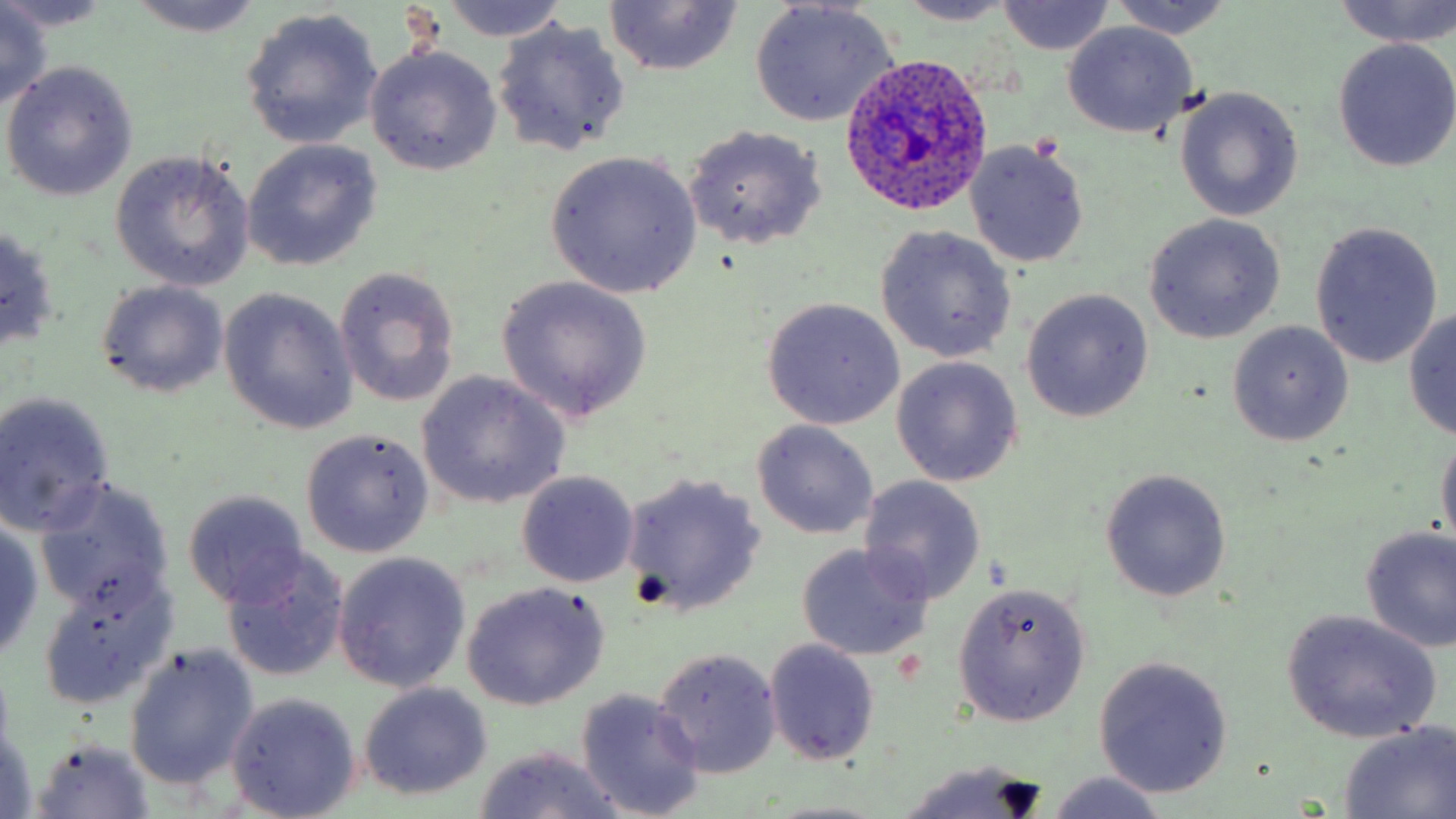 Approximate bounding boxes as [x1, y1, x2, y2] in pixels. Uninfected red blood cell locations: [123, 0, 264, 38], [1106, 0, 1238, 40], [0, 1, 113, 34], [436, 1, 574, 43], [1333, 1, 1456, 49], [602, 2, 742, 76], [895, 2, 1019, 26], [998, 2, 1113, 54], [0, 3, 53, 109], [750, 4, 898, 125], [239, 8, 385, 150], [491, 20, 630, 158], [1062, 22, 1197, 137], [1331, 39, 1456, 174], [365, 44, 502, 176], [3, 60, 139, 200], [1175, 89, 1302, 219], [682, 124, 828, 250], [964, 138, 1091, 269], [243, 140, 382, 271], [111, 150, 255, 291], [545, 151, 702, 299], [1143, 214, 1285, 343], [1308, 221, 1443, 370], [0, 225, 61, 353], [874, 226, 1016, 363], [335, 267, 460, 407], [495, 275, 654, 422], [96, 280, 230, 399], [1021, 288, 1154, 423], [219, 289, 359, 436], [761, 298, 905, 431], [1402, 307, 1456, 437], [1227, 322, 1354, 447], [891, 356, 1024, 487], [416, 372, 568, 509], [0, 393, 116, 537], [749, 419, 879, 540], [301, 429, 434, 558], [1436, 431, 1456, 557], [1099, 468, 1232, 603], [516, 471, 639, 587], [621, 473, 766, 619], [858, 475, 987, 604], [37, 480, 174, 618], [182, 489, 310, 610], [0, 517, 46, 665], [1357, 525, 1456, 654], [796, 543, 934, 662], [223, 552, 348, 682], [332, 552, 470, 694], [38, 577, 171, 708], [953, 582, 1090, 727], [464, 583, 608, 710], [1281, 609, 1442, 744], [764, 638, 881, 766], [123, 643, 260, 790], [652, 647, 782, 778], [1092, 656, 1234, 799], [359, 683, 494, 802], [577, 689, 707, 819], [226, 693, 360, 818], [2, 723, 43, 819], [1336, 723, 1456, 817], [32, 737, 155, 818], [473, 745, 626, 819], [894, 757, 1050, 819], [1046, 773, 1169, 819]. Plasmodium ovale-infected red blood cell locations: [838, 52, 993, 216]. Slide-level diagnosis: Plasmodium ovale. Optical microscopy. May-Grünwald-Giemsa stain. Single field of view. Image is 1456×819 pixels. Thin blood film. Captured at 1000x magnification.